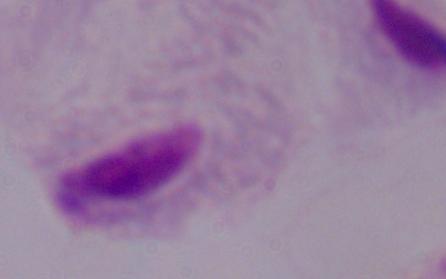
{
  "magnification": "1000x",
  "modality": "photomicrograph",
  "identification": "trichomonad"
}